Evaluate for Plasmodium parasites.
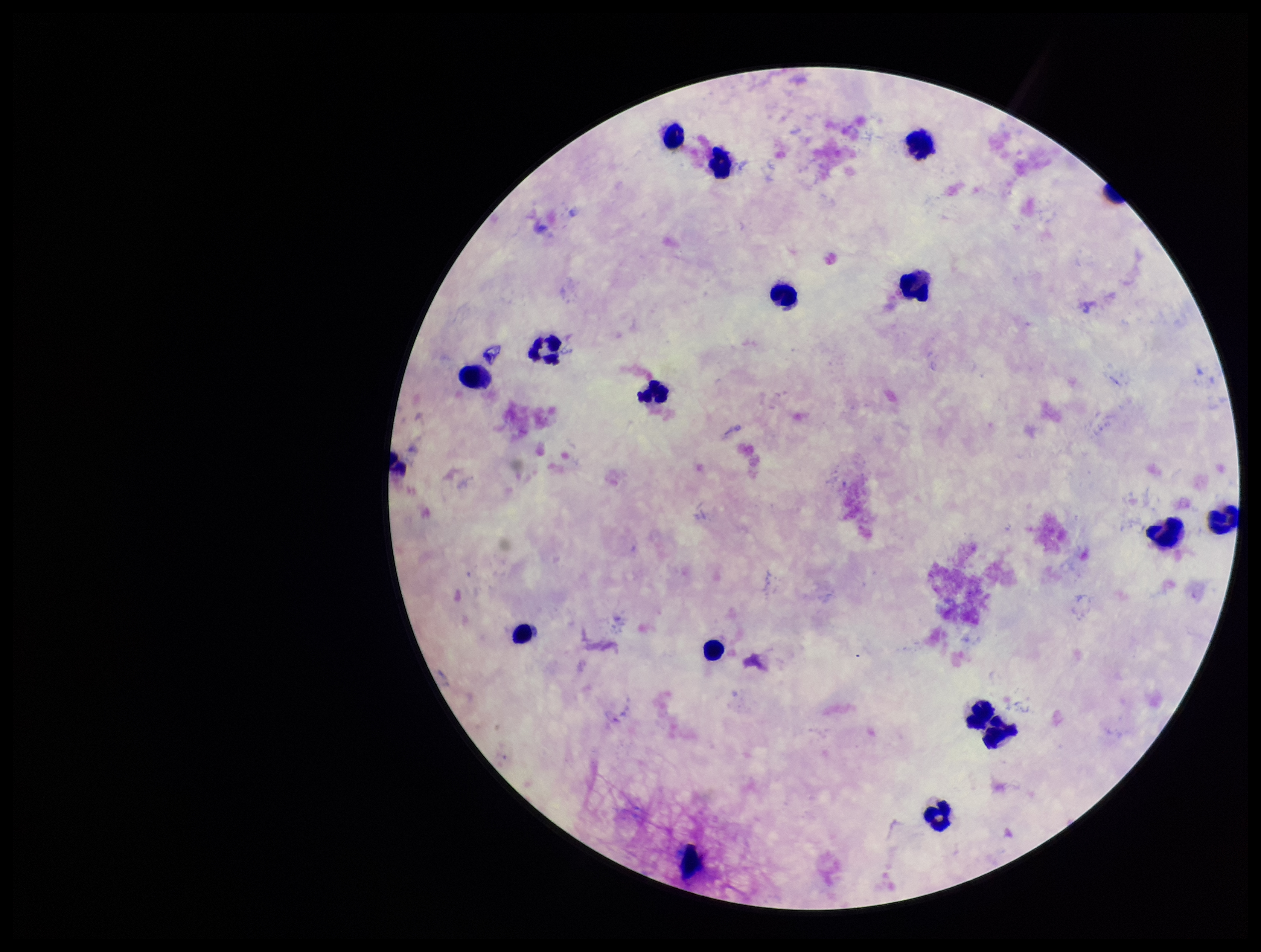

None detected.

patient malaria status = negative
parasite count = 0
image size = 1261×952 pixels
leukocyte count = 16
stain = Giemsa
capture = smartphone photograph through the microscope eyepiece
field of view = single
preparation = thick blood smear